State the blood parasite species.
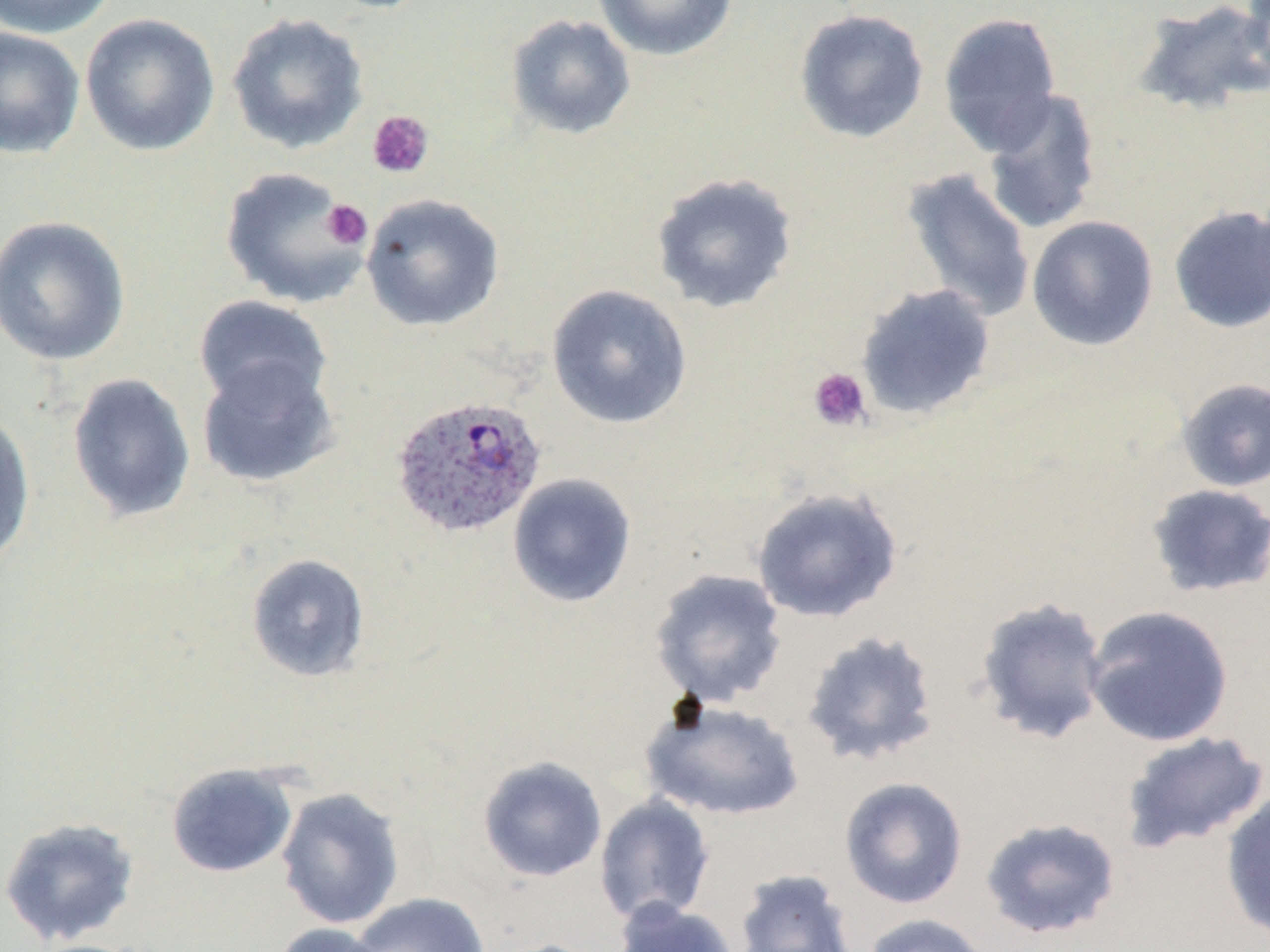
Plasmodium ovale.

Summary:
  - Coordinate format: approximate bounding boxes as (x1,y1)-(x2,y2) corner pairs in pixels
  - Uninfected red blood cell locations: (0,0)-(119,39), (592,0)-(740,61), (1241,0)-(1270,82), (1132,1)-(1270,116), (793,8)-(929,144), (226,12)-(369,155), (938,12)-(1062,155), (79,13)-(220,156), (505,13)-(636,140), (0,27)-(85,159), (981,87)-(1102,235), (220,166)-(368,309), (900,168)-(1037,323), (650,172)-(799,314), (361,193)-(505,332), (1168,204)-(1270,334), (0,215)-(131,365), (1026,215)-(1159,351), (856,283)-(996,420), (546,284)-(693,429), (193,294)-(332,413), (196,356)-(341,489), (66,372)-(196,523), (1176,377)-(1270,492), (0,409)-(36,570), (507,472)-(637,608), (1146,484)-(1270,598), (750,486)-(904,623), (246,553)-(371,682), (648,568)-(788,709), (974,596)-(1111,745), (1083,604)-(1234,747), (800,629)-(942,767), (640,698)-(805,822), (1119,731)-(1270,854), (477,756)-(608,882), (165,762)-(298,878), (839,776)-(969,909), (276,787)-(405,929), (1220,788)-(1270,944), (593,794)-(715,925), (0,816)-(140,948), (979,816)-(1122,940), (733,869)-(859,952), (350,892)-(490,952), (614,899)-(742,952), (860,913)-(994,952), (269,922)-(393,952), (487,938)-(611,952)
  - Plasmodium ovale-infected red blood cell locations: (389,393)-(547,540)
  - Platelet locations: (367,109)-(435,180), (322,200)-(372,249), (808,367)-(873,432)
  - Modality: optical microscopy
  - Preparation: thin blood smear
  - Stain: May-Grünwald-Giemsa
  - Field of view: one of a larger specimen
  - Magnification: 1000x
  - Image size: 1270×952 pixels